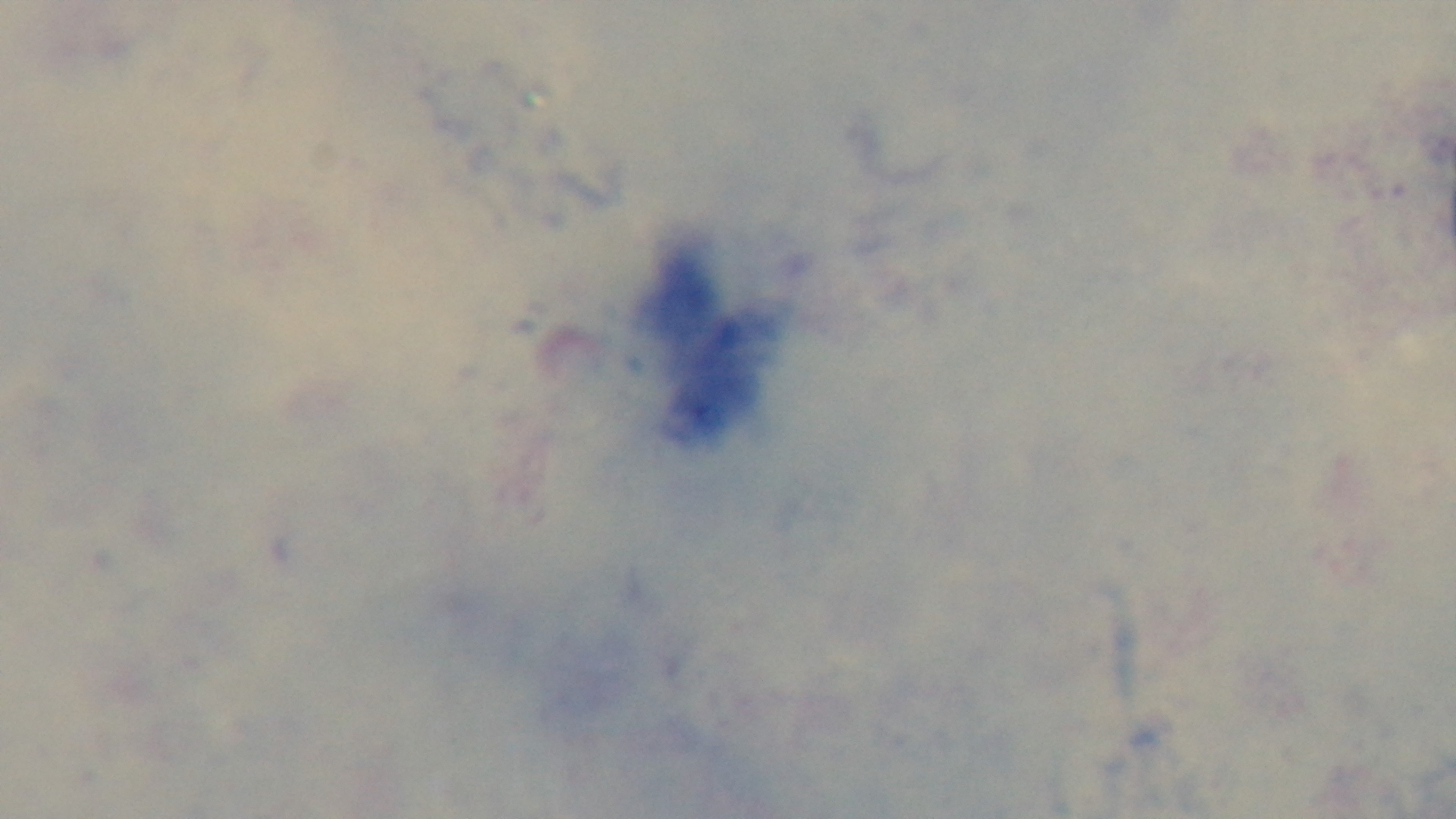

modality = light microscopy
field of view = single
capture = mounted 4K digital camera
stain = Giemsa
malaria status = negative
objective = 100x oil immersion
preparation = thick smear